Report the malaria status of this cell.
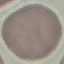

It is uninfected.

Summary:
  - Capture: smartphone through the microscope eyepiece
  - Preparation: thin blood smear
  - Image type: cell patch, automatically extracted from a larger field of view and resized to 64 × 64 pixels
  - Stain: Giemsa